Identify the blood parasite species.
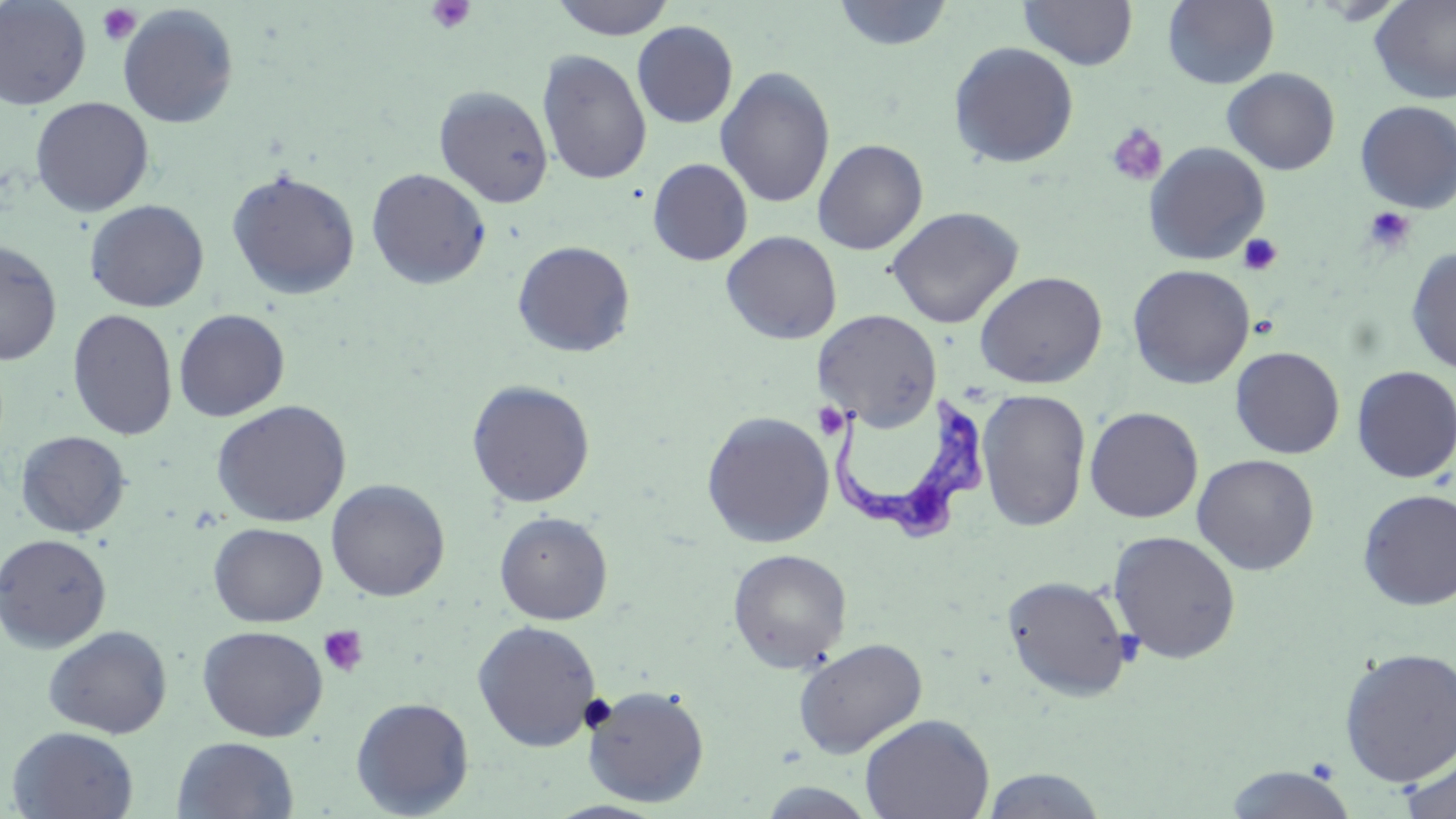
Trypanosoma brucei.

Summary:
  - Coordinate format: approximate bounding boxes as [x1, y1, x2, y2] in pixels
  - Platelet locations: [426, 0, 475, 35], [96, 3, 142, 46], [1106, 123, 1169, 187], [1363, 206, 1417, 254], [1238, 233, 1282, 276], [812, 402, 850, 440], [318, 625, 369, 678], [579, 693, 617, 733]
  - Uninfected red blood cell locations: [0, 0, 92, 110], [550, 0, 676, 40], [830, 0, 955, 52], [1018, 0, 1138, 71], [1162, 0, 1280, 89], [1369, 0, 1456, 104], [117, 4, 239, 129], [632, 21, 738, 128], [948, 41, 1080, 168], [537, 49, 652, 185], [715, 66, 835, 209], [1222, 67, 1341, 175], [434, 86, 554, 207], [30, 97, 154, 217], [1354, 100, 1456, 213], [812, 139, 928, 255], [1143, 142, 1271, 265], [647, 157, 753, 266], [226, 168, 362, 300], [366, 168, 491, 289], [84, 199, 209, 312], [885, 206, 1024, 329], [720, 231, 842, 345], [0, 240, 62, 366], [512, 240, 635, 358], [1406, 247, 1456, 376], [1127, 264, 1255, 389], [974, 271, 1108, 389], [67, 308, 178, 440], [173, 308, 290, 422], [814, 309, 941, 431], [1230, 346, 1345, 459], [1352, 365, 1456, 483], [466, 379, 595, 508], [976, 388, 1091, 532], [211, 399, 351, 527], [1084, 406, 1204, 523], [701, 410, 835, 548], [15, 431, 131, 538], [1192, 453, 1320, 575], [325, 479, 450, 602], [1357, 488, 1456, 610], [494, 511, 613, 625], [208, 522, 328, 627], [1107, 530, 1242, 664], [0, 533, 112, 652], [727, 548, 852, 672], [1001, 574, 1134, 702], [472, 620, 602, 751], [43, 625, 172, 738], [197, 625, 328, 741], [792, 636, 928, 758], [1338, 646, 1456, 787], [584, 684, 710, 807], [350, 697, 475, 817], [860, 713, 994, 819], [6, 726, 140, 818], [172, 736, 299, 819], [1397, 748, 1456, 819], [1223, 765, 1359, 819], [978, 768, 1111, 818], [754, 781, 882, 819]
  - Trypanosoma brucei locations: [831, 388, 985, 544]
  - Field of view: single
  - Preparation: thin blood film
  - Magnification: 1000x
  - Stain: May-Grünwald-Giemsa
  - Image size: 1456×819 pixels
  - Modality: optical microscopy